Point out each Plasmodium parasite.
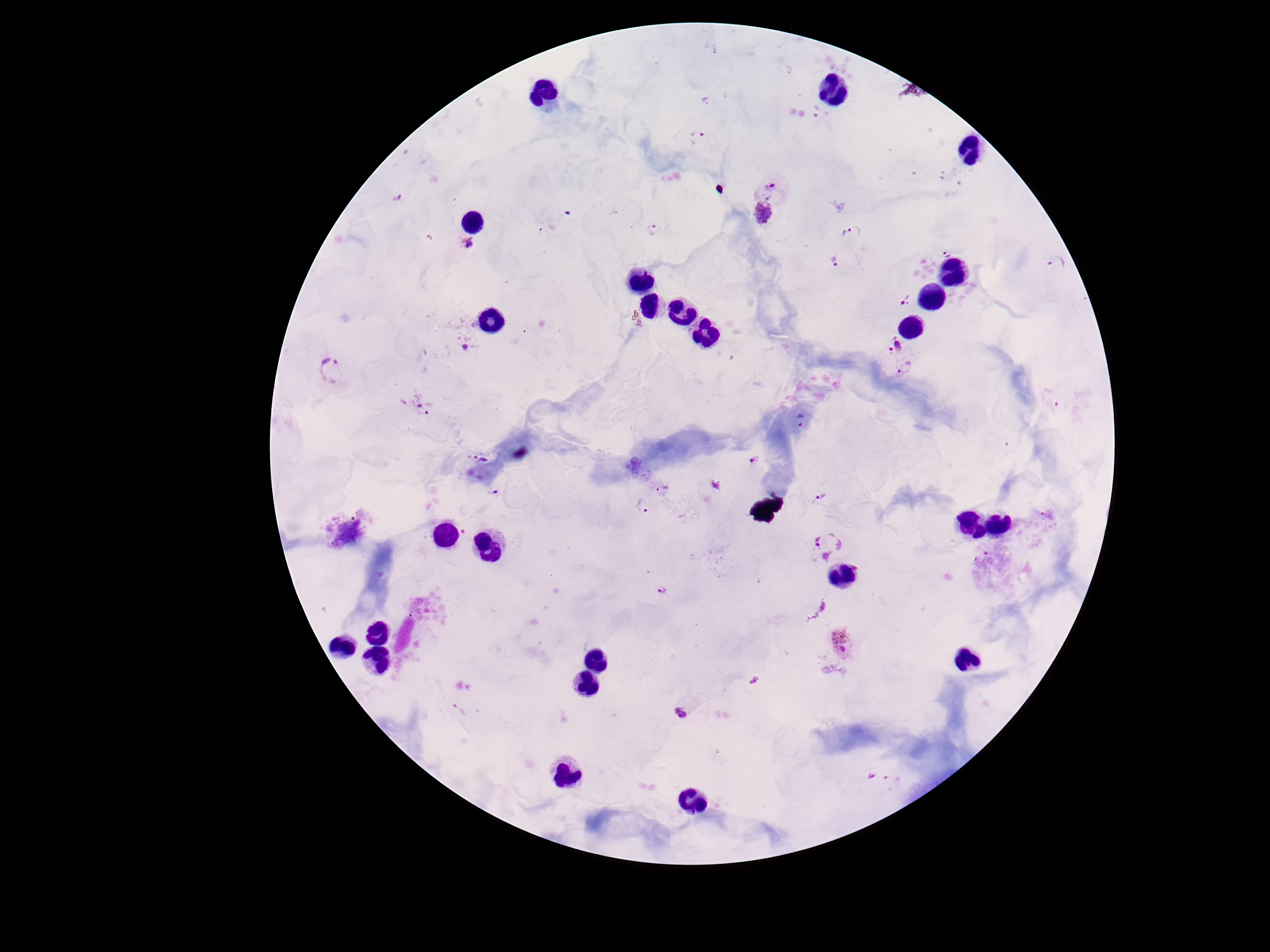
Approximate centers as {x, y} in pixels.
Plasmodium parasites: {819, 114}, {699, 138}, {769, 190}, {397, 198}, {763, 213}, {655, 231}, {848, 233}, {466, 243}, {946, 250}, {836, 261}, {1057, 264}, {904, 301}, {895, 345}, {465, 349}, {907, 368}, {331, 372}, {418, 406}, {801, 422}, {754, 460}, {662, 489}, {820, 498}, {642, 505}, {350, 534}, {826, 544}, {662, 590}, {843, 641}, {681, 713}.

Summary:
  - Preparation: thick blood smear
  - Stain: Giemsa
  - Field of view: single
  - Capture: smartphone camera through the microscope eyepiece
  - Image size: 1270×952 pixels
  - Patient malaria status: infected
  - Magnification: 100x